Point out each Plasmodium parasite.
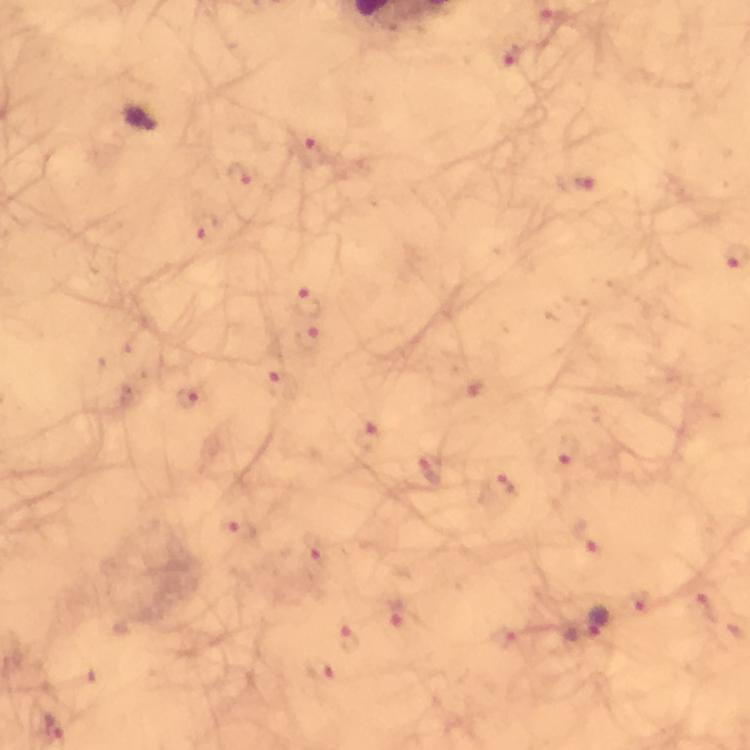
Approximate centers as {x, y} in pixels.
Plasmodium parasites: {507, 55}, {313, 149}, {238, 177}, {574, 181}, {206, 226}, {308, 301}, {309, 338}, {282, 384}, {474, 389}, {192, 396}, {368, 437}, {562, 457}, {432, 468}, {500, 489}, {237, 531}, {587, 538}, {314, 551}, {703, 603}, {643, 605}, {396, 612}, {599, 622}, {351, 638}, {503, 638}, {322, 668}.

context = from a diagnostic examination for malaria
image size = 750×750 pixels
preparation = thick blood smear
immersion oil = used
stain = Giemsa
magnification = 100x
cropped from = a single field of view
capture = smartphone photograph through a microscope